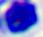
magnification: 400x
identification: leukocyte
modality: micrograph